State which parasite is depicted.
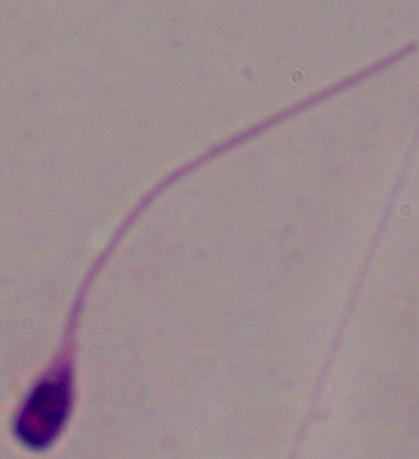

This is Leishmania.

Captured at 1000x magnification. Photomicrograph.